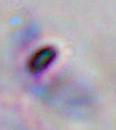
identification: Toxoplasma gondii
magnification: 1000x
modality: micrograph